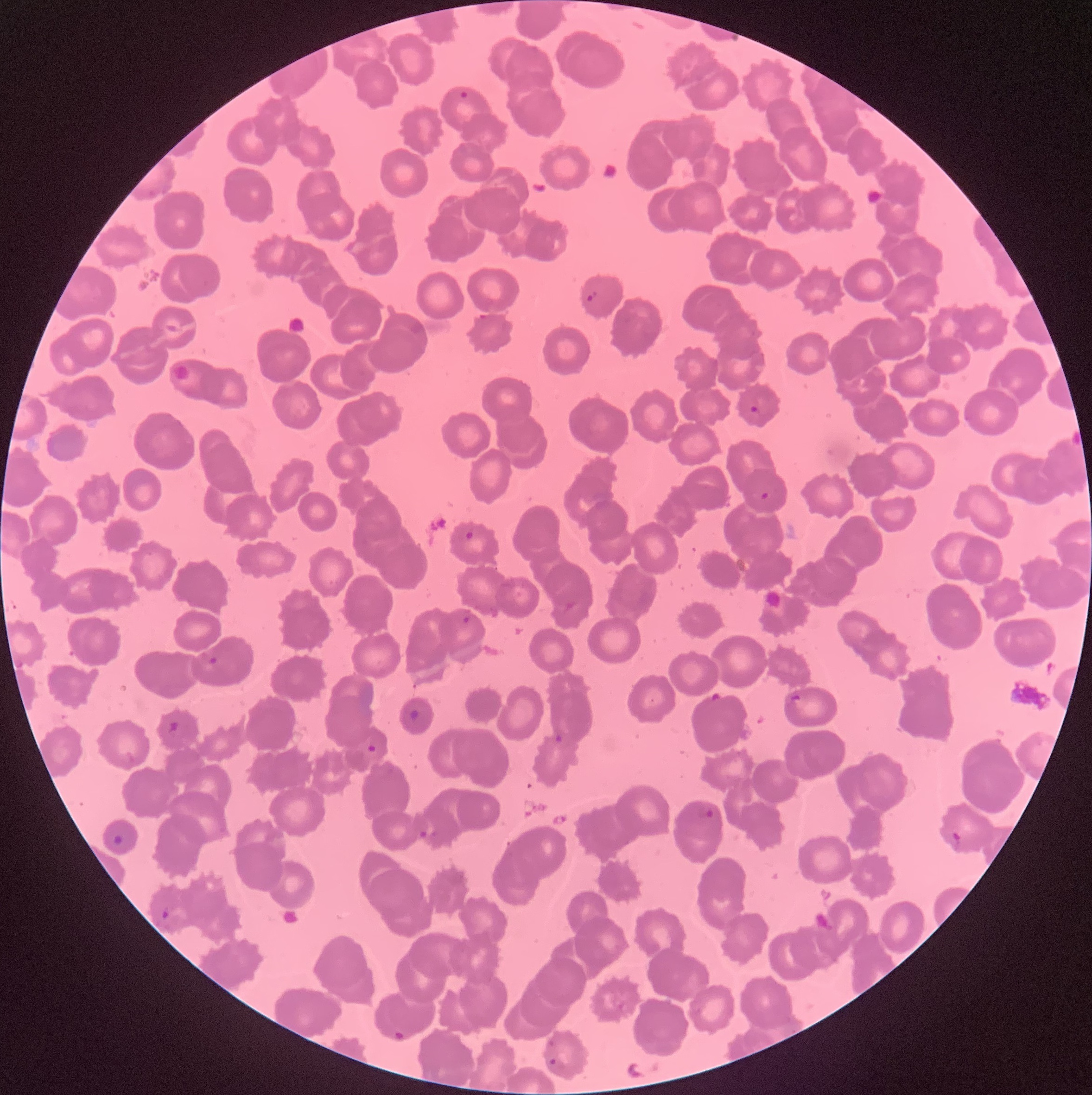
preparation: thin blood smear
modality: light microscopy
image_size: 1092×1095 pixels
red_blood_cell_morphology: rouleaux formation
plasmodium_parasite_locations: 'approximate bounding boxes as (x1,y1)-(x2,y2) corner pairs in pixels: (458,89)-(469,99), (586,290)-(598,302), (749,404)-(758,413), (757,490)-(772,502), (463,530)-(476,542), (461,615)-(472,625), (207,656)-(219,666), (709,691)-(728,705), (788,695)-(809,714), (552,734)-(565,745), (364,743)-(380,756), (697,806)-(715,822), (418,828)-(440,841), (949,831)-(962,849), (159,907)-(174,923), (392,1029)-(406,1044), (545,1058)-(566,1075)'